Assess this cell for malaria.
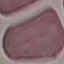
Uninfected.

image type = cell patch, automatically extracted from a larger field of view and resized to 64 × 64 pixels
stain = Giemsa
capture = smartphone through the microscope eyepiece
preparation = thin blood film